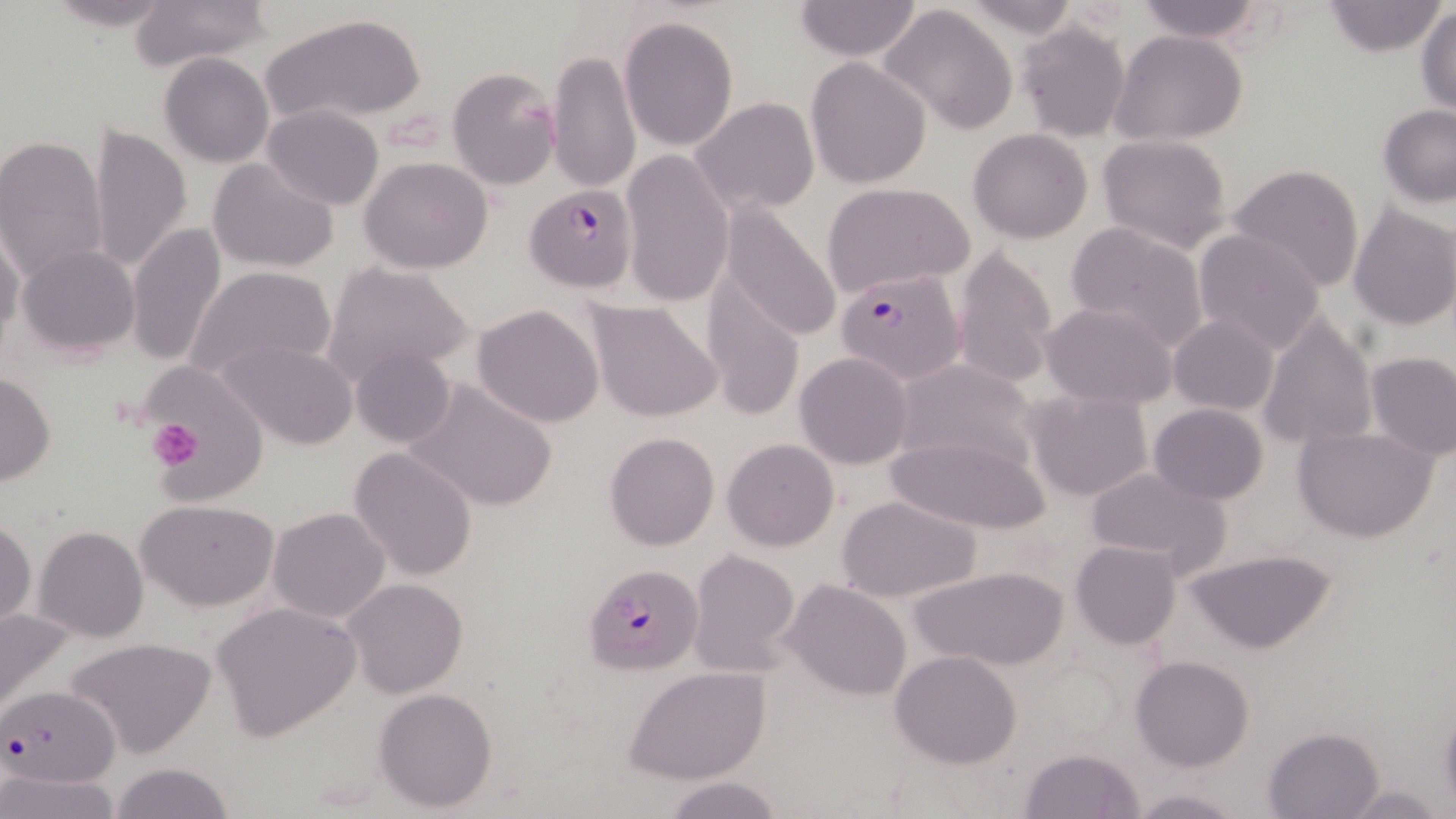
Approximate bounding boxes as (x1,y1)-(x2,y2) corner pairs in pixels. Plasmodium falciparum-infected red blood cell locations: (524,186)-(636,293), (834,264)-(967,385), (582,563)-(703,674), (1,687)-(120,790). Platelet locations: (149,418)-(202,468). Uninfected red blood cell locations: (41,0)-(179,31), (130,0)-(270,72), (791,0)-(925,61), (1132,0)-(1271,43), (956,1)-(1081,40), (1322,1)-(1443,56), (879,3)-(1019,135), (1416,4)-(1456,115), (260,12)-(429,128), (618,14)-(740,152), (1015,18)-(1132,142), (1110,30)-(1249,147), (546,47)-(640,196), (159,53)-(274,169), (805,57)-(933,190), (446,67)-(560,191), (691,98)-(820,218), (262,104)-(385,210), (1378,104)-(1456,206), (88,124)-(192,273), (967,129)-(1093,244), (0,134)-(109,283), (1097,134)-(1234,253), (620,148)-(734,308), (360,156)-(494,274), (209,158)-(338,274), (1228,164)-(1365,290), (821,182)-(974,296), (719,202)-(844,343), (1348,202)-(1456,331), (125,220)-(227,369), (1064,221)-(1209,352), (0,226)-(25,356), (1193,228)-(1327,354), (947,244)-(1059,388), (16,246)-(142,359), (323,262)-(473,386), (184,263)-(336,387), (700,270)-(806,422), (585,299)-(724,424), (1042,302)-(1178,410), (472,303)-(604,428), (1169,314)-(1279,416), (1257,314)-(1378,452), (216,337)-(360,450), (350,346)-(457,448), (794,351)-(913,469), (1364,352)-(1455,461), (891,358)-(1038,470), (1,372)-(56,486), (145,373)-(265,501), (405,376)-(560,513), (1024,388)-(1154,503), (1150,402)-(1268,504), (1292,423)-(1440,542), (603,431)-(720,550), (885,433)-(1048,533), (721,438)-(838,551), (348,446)-(478,580), (1083,465)-(1232,574), (836,494)-(983,605), (137,496)-(279,610), (267,507)-(391,625), (0,517)-(36,636), (33,527)-(149,644), (1068,541)-(1181,650), (1187,548)-(1337,655), (686,549)-(802,678), (909,566)-(1068,673), (343,578)-(470,697), (781,579)-(912,701), (211,601)-(362,743), (1,607)-(75,722), (63,636)-(219,759), (890,650)-(1023,769), (1130,654)-(1253,771), (626,666)-(772,784), (372,686)-(499,813), (1439,699)-(1456,811), (1262,726)-(1384,818), (1016,746)-(1145,818), (108,760)-(238,818), (0,770)-(122,819), (663,776)-(788,819), (1339,783)-(1449,817), (1128,788)-(1244,818). Slide-level diagnosis: Plasmodium falciparum. Optical microscopy. Image is 1456×819 pixels. 1000x magnification. Single field of view. May-Grünwald-Giemsa-stained preparation. Thin blood smear.